Classify this cell by malaria status.
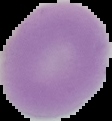

Uninfected.

image type = cell region segmented out of the field of view; surrounding area masked to black
image size = 112×121 pixels
preparation = thin blood film